Assess this cell for malaria.
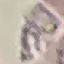
Uninfected.

preparation = thin blood film
capture = smartphone camera at the microscope eyepiece
stain = Giemsa
image type = automatically extracted cell patch, resized to 64 × 64 pixels